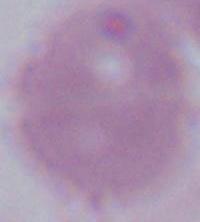
identification = red blood cell
magnification = 1000x
modality = photomicrograph